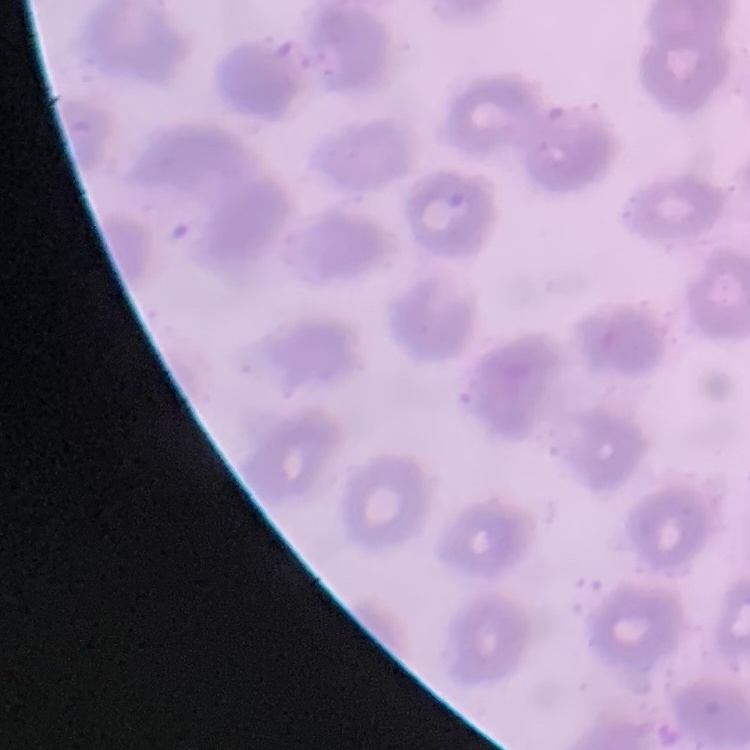

Summary:
  - Erythrocyte morphology: no rouleaux formation
  - Image type: one tile cut from a larger photomicrograph
  - Preparation: thin blood film
  - Stain: Field's or Giemsa